Identify the blood parasite species.
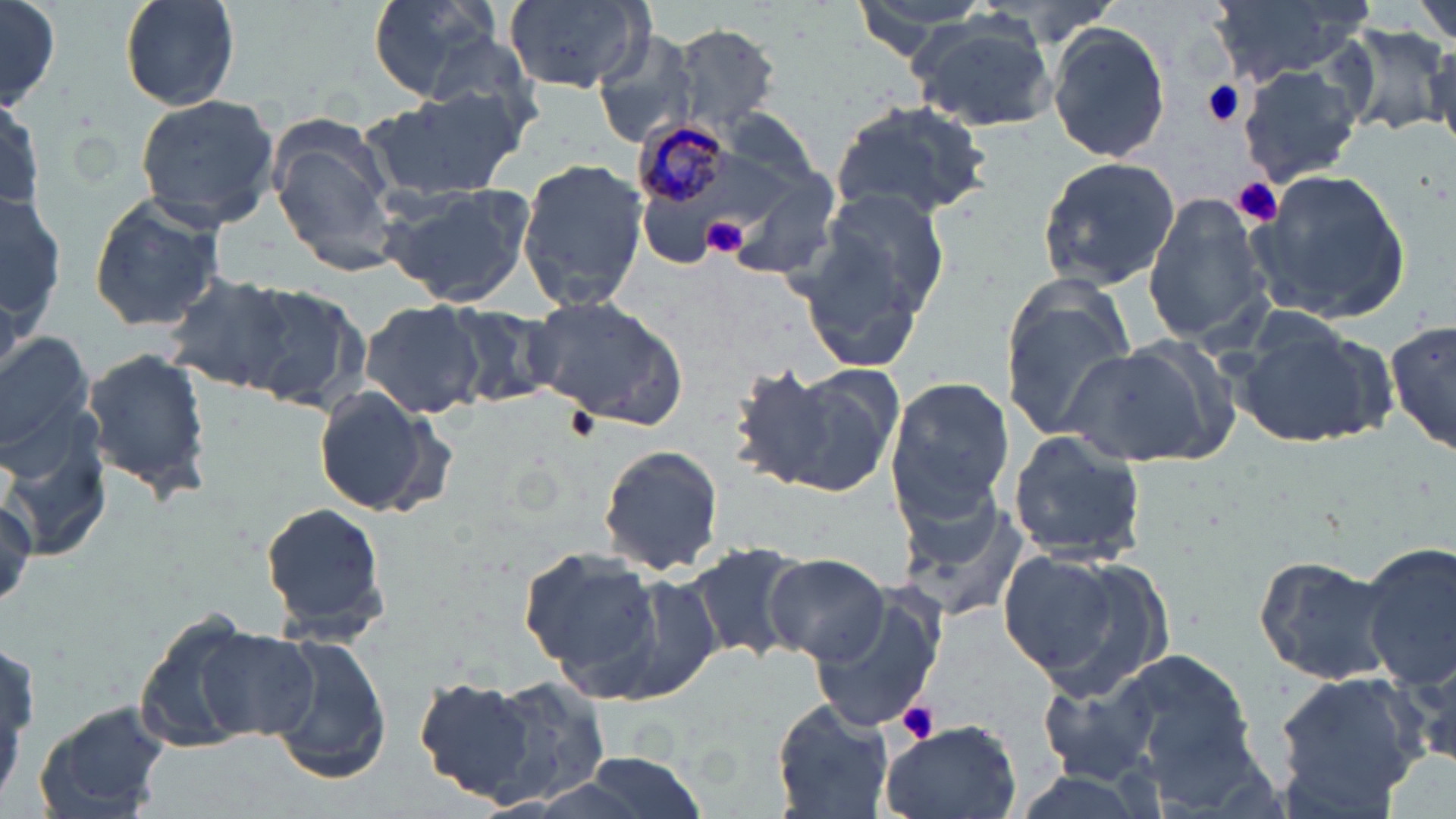

Plasmodium malariae.

magnification = 1000x
preparation = thin blood smear
Plasmodium malariae-infected red blood cell locations = approximate bounding boxes as (x1, y1, x2, y2) in pixels: (629, 117, 736, 215)
modality = light microscopy
image size = 1456×819 pixels
field of view = one of a larger specimen
stain = May-Grünwald-Giemsa
uninfected red blood cell locations = approximate bounding boxes as (x1, y1, x2, y2) in pixels: (0, 0, 62, 109), (117, 0, 242, 111), (366, 0, 500, 104), (501, 0, 651, 93), (846, 0, 999, 61), (1412, 0, 1456, 46), (1214, 1, 1374, 86), (907, 17, 1059, 135), (1045, 20, 1171, 166), (664, 22, 783, 134), (1341, 24, 1450, 139), (590, 27, 700, 149), (414, 28, 544, 135), (1238, 63, 1365, 189), (359, 86, 529, 205), (132, 93, 282, 227), (1, 95, 44, 220), (830, 96, 994, 222), (719, 107, 825, 190), (267, 119, 404, 276), (515, 157, 651, 313), (1034, 157, 1180, 290), (1245, 167, 1414, 325), (723, 168, 843, 281), (378, 183, 535, 309), (2, 185, 65, 350), (814, 185, 952, 323), (1141, 190, 1276, 347), (86, 192, 227, 333), (793, 224, 936, 372), (164, 273, 299, 396), (239, 281, 372, 412), (1000, 285, 1137, 442), (522, 294, 691, 429), (360, 300, 486, 421), (439, 302, 564, 410), (1229, 313, 1394, 452), (1385, 314, 1456, 461), (0, 328, 96, 462), (1068, 337, 1242, 469), (81, 348, 213, 503), (734, 362, 900, 498), (884, 375, 1015, 529), (310, 383, 450, 521), (2, 408, 115, 560), (1007, 431, 1150, 564), (596, 445, 726, 577), (894, 486, 1035, 627), (260, 499, 390, 642), (1361, 538, 1456, 691), (685, 540, 811, 665), (519, 548, 663, 684), (998, 548, 1166, 695), (1251, 553, 1397, 686), (764, 554, 891, 667), (600, 570, 726, 703), (804, 587, 948, 735), (132, 615, 268, 745), (196, 629, 322, 741), (260, 631, 392, 783), (1102, 647, 1260, 779), (1270, 665, 1429, 814), (1038, 667, 1167, 783), (408, 672, 548, 799), (472, 679, 615, 807), (768, 697, 896, 819), (35, 702, 172, 819), (877, 717, 1024, 819), (572, 750, 710, 819)
platelet locations = approximate bounding boxes as (x1, y1, x2, y2) in pixels: (1200, 78, 1247, 129), (1234, 179, 1284, 226), (702, 215, 747, 258), (894, 700, 942, 745)